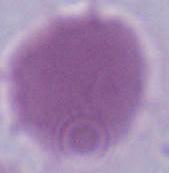
modality = micrograph
magnification = 1000x
identification = erythrocyte